Outline platelets.
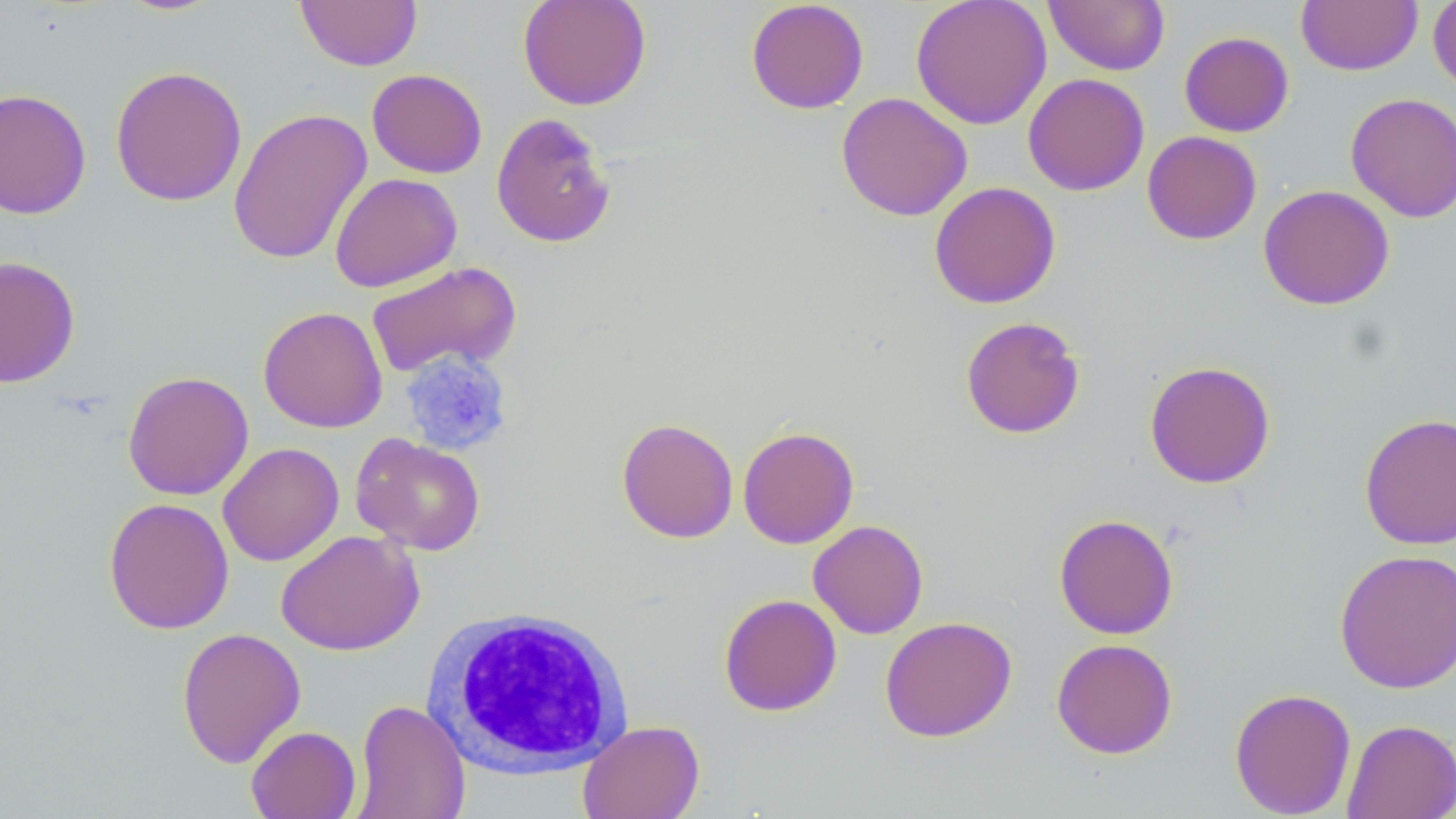
Approximate bounding boxes as [x1, y1, x2, y2] in pixels.
Platelets: [400, 351, 513, 455].

slide-level diagnosis = negative for blood parasites
white blood cell locations = approximate bounding boxes as [x1, y1, x2, y2] in pixels: [422, 607, 634, 779]
field of view = single
preparation = thin blood film
uninfected red blood cell locations = approximate bounding boxes as [x1, y1, x2, y2] in pixels: [114, 0, 225, 17], [295, 0, 423, 71], [517, 0, 652, 111], [745, 0, 869, 114], [910, 0, 1051, 130], [1044, 0, 1170, 75], [1296, 0, 1423, 76], [1428, 0, 1456, 96], [1178, 31, 1294, 137], [109, 65, 247, 207], [367, 68, 488, 179], [1023, 73, 1150, 196], [0, 88, 92, 220], [835, 92, 973, 221], [1345, 92, 1456, 222], [228, 108, 372, 265], [491, 112, 617, 248], [1141, 130, 1262, 245], [329, 172, 462, 292], [929, 181, 1061, 309], [1258, 184, 1395, 311], [0, 255, 81, 388], [365, 261, 521, 378], [258, 306, 388, 433], [960, 316, 1086, 439], [1144, 360, 1275, 489], [122, 370, 254, 500], [1359, 412, 1456, 550], [616, 417, 739, 543], [737, 426, 858, 548], [351, 433, 486, 555], [218, 442, 344, 566], [103, 497, 234, 635], [1053, 513, 1179, 639], [808, 519, 929, 639], [276, 529, 424, 656], [1334, 549, 1456, 694], [718, 593, 842, 717], [879, 616, 1017, 742], [176, 626, 306, 769], [1051, 638, 1178, 759], [1229, 687, 1357, 818], [352, 699, 471, 819], [1342, 718, 1456, 818], [577, 719, 705, 819], [245, 725, 361, 819]
modality = light microscopy
magnification = 1000x
stain = May-Grünwald-Giemsa
image size = 1456×819 pixels